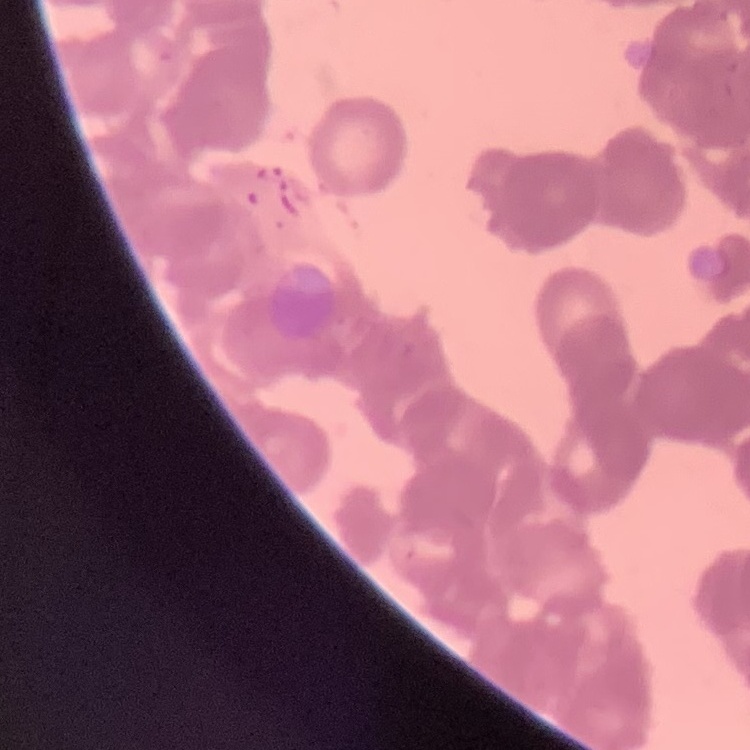

Summary:
  - Red blood cell morphology: rouleaux formation
  - Image type: one tile cut from a larger photomicrograph
  - Preparation: thin blood film
  - Stain: Field's or Giemsa